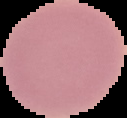 Malaria status: uninfected. Image is 127×118 pixels. From a thin blood smear. The area outside the segmented cell region is set to black.